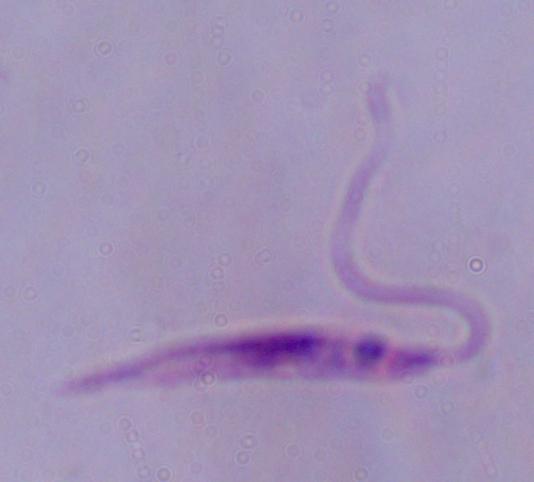

Photomicrograph. A Leishmania parasite is seen. 1000x magnification.